Locate and identify every blood parasite.
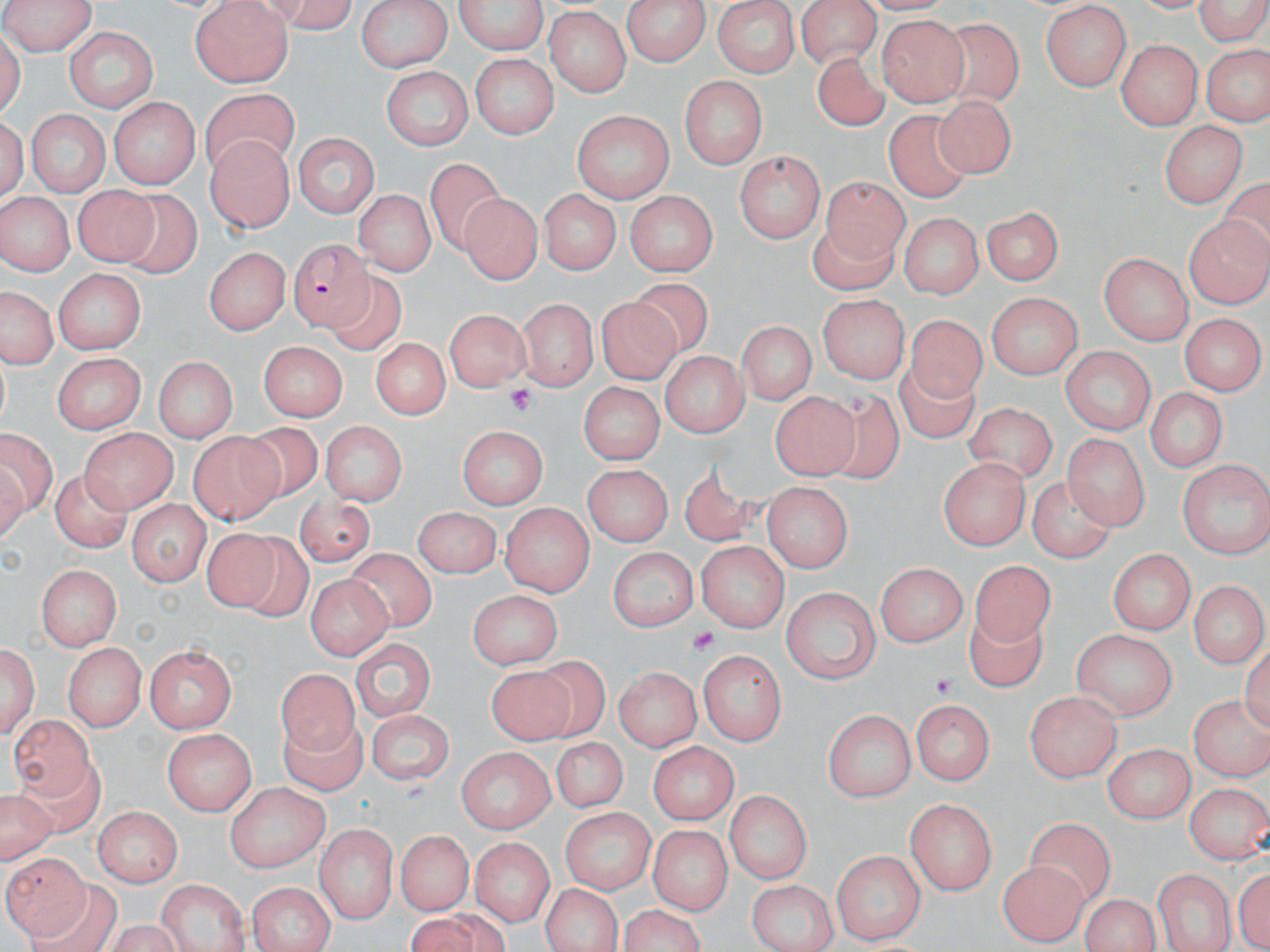
Approximate bounding boxes as [x1, y1, x2, y2] in pixels.
Plasmodium falciparum-infected red blood cells: [287, 238, 382, 337].
No Plasmodium ovale, Plasmodium malariae, Plasmodium vivax, Babesia divergens, or Trypanosoma brucei observed.

Summary:
  - Platelet locations: [503, 383, 536, 415], [689, 626, 721, 658], [929, 671, 959, 698]
  - Uninfected red blood cell locations: [0, 0, 100, 54], [258, 0, 358, 30], [354, 0, 453, 72], [452, 0, 549, 56], [621, 0, 714, 65], [710, 0, 801, 77], [795, 0, 884, 64], [1190, 0, 1270, 45], [190, 1, 295, 88], [1039, 5, 1133, 89], [544, 8, 631, 97], [876, 17, 969, 107], [944, 22, 1025, 107], [60, 30, 157, 109], [1116, 40, 1203, 125], [1205, 45, 1266, 120], [815, 52, 888, 130], [468, 53, 560, 137], [384, 68, 471, 154], [679, 74, 767, 170], [200, 90, 304, 178], [110, 102, 202, 192], [935, 103, 1014, 182], [24, 108, 111, 200], [571, 110, 675, 204], [888, 111, 971, 204], [1159, 122, 1246, 207], [203, 135, 295, 236], [293, 135, 380, 218], [735, 152, 823, 242], [424, 153, 513, 256], [822, 177, 906, 265], [73, 183, 157, 266], [538, 188, 619, 277], [355, 190, 433, 278], [0, 191, 74, 279], [126, 191, 201, 282], [627, 192, 718, 277], [460, 194, 538, 285], [980, 204, 1062, 289], [897, 212, 985, 296], [1184, 213, 1270, 307], [808, 221, 898, 293], [201, 245, 288, 334], [1102, 249, 1198, 338], [49, 268, 147, 357], [340, 278, 412, 363], [627, 279, 715, 353], [2, 289, 52, 367], [519, 294, 596, 386], [597, 294, 681, 391], [983, 294, 1083, 377], [816, 295, 907, 382], [442, 311, 528, 392], [908, 315, 987, 406], [1178, 315, 1264, 394], [739, 321, 813, 408], [371, 333, 451, 420], [260, 340, 349, 421], [1061, 346, 1156, 436], [53, 352, 144, 434], [659, 352, 750, 437], [149, 354, 240, 442], [898, 359, 981, 447], [576, 382, 660, 464], [1144, 385, 1229, 471], [771, 389, 857, 479], [824, 390, 901, 487], [964, 405, 1057, 488], [321, 423, 407, 506], [83, 425, 180, 510], [234, 425, 324, 497], [456, 425, 547, 510], [0, 429, 57, 522], [1062, 431, 1148, 528], [188, 432, 279, 522], [1177, 454, 1269, 558], [938, 456, 1034, 548], [583, 462, 674, 547], [676, 465, 774, 546], [48, 470, 128, 554], [1031, 478, 1112, 562], [763, 484, 852, 572], [292, 491, 377, 571], [125, 500, 209, 584], [501, 501, 591, 596], [413, 506, 500, 576], [205, 525, 283, 615], [241, 534, 309, 627], [697, 542, 787, 632], [606, 547, 698, 628], [1106, 547, 1193, 635], [353, 549, 447, 637], [969, 561, 1057, 654], [38, 562, 122, 649], [875, 563, 968, 645], [50, 574, 135, 706], [307, 574, 393, 661], [1185, 578, 1270, 669], [782, 585, 882, 683], [467, 589, 561, 670], [965, 610, 1042, 690], [1073, 630, 1176, 722], [352, 638, 434, 724], [1, 640, 40, 742], [144, 642, 238, 734], [61, 644, 145, 730], [699, 650, 786, 745], [535, 657, 611, 739], [486, 665, 575, 746], [615, 665, 700, 754], [275, 672, 372, 756], [1024, 689, 1120, 781], [1187, 691, 1269, 779], [912, 696, 993, 786], [366, 709, 456, 787], [824, 710, 915, 804], [14, 713, 101, 800], [272, 714, 369, 798], [164, 729, 256, 814], [548, 737, 627, 813], [646, 738, 738, 826], [1100, 741, 1194, 821], [456, 747, 557, 836], [10, 761, 107, 839], [223, 782, 328, 870], [1185, 782, 1270, 862], [726, 789, 812, 887], [905, 799, 997, 897], [92, 808, 181, 888], [558, 808, 656, 897], [1027, 818, 1113, 907], [313, 825, 396, 921], [650, 825, 731, 917], [393, 829, 478, 913], [470, 834, 552, 926], [832, 847, 925, 945], [4, 852, 84, 939], [996, 859, 1088, 944], [1233, 860, 1270, 952], [1153, 868, 1235, 952], [746, 878, 841, 952], [31, 879, 120, 952], [155, 879, 248, 952], [247, 880, 331, 952], [538, 884, 627, 951], [1076, 892, 1167, 950], [616, 906, 704, 952], [409, 914, 480, 951]
  - Slide-level diagnosis: Plasmodium falciparum
  - Preparation: thin blood smear
  - Field of view: one of a larger specimen
  - Stain: May-Grünwald-Giemsa
  - Modality: light microscopy
  - Image size: 1270×952 pixels
  - Magnification: 1000x